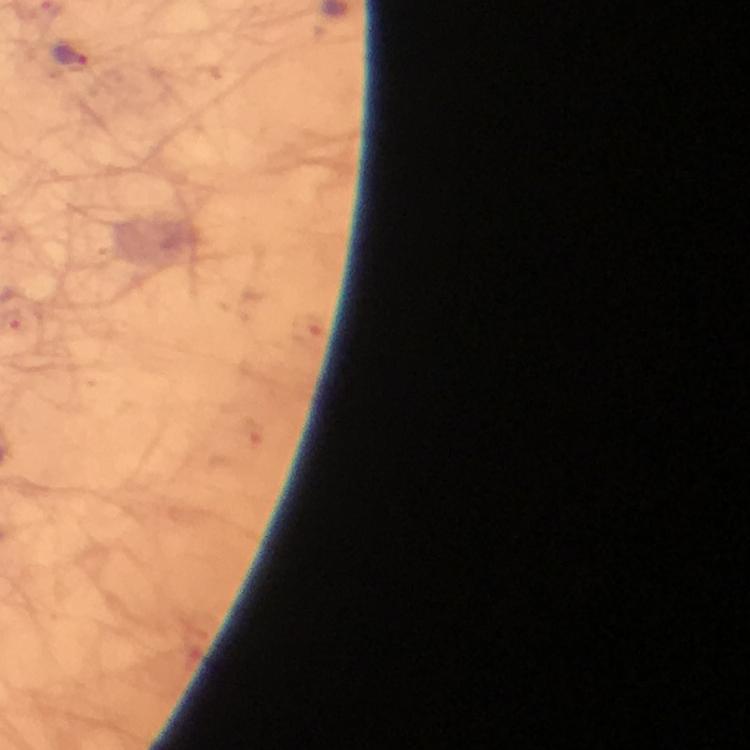
Approximate object centers, in pixels from the top-left corner.
Summary:
  - Malaria parasite locations: (x=72, y=55)
  - Context: from a diagnostic examination for malaria
  - Immersion oil: used
  - Magnification: 100x
  - Capture: smartphone camera through the microscope
  - Cropped from: a single field of view
  - Stain: Giemsa
  - Image size: 750×750 pixels
  - Preparation: thick smear